Give the extent of all Plasmodium falciparum-infected red blood cells.
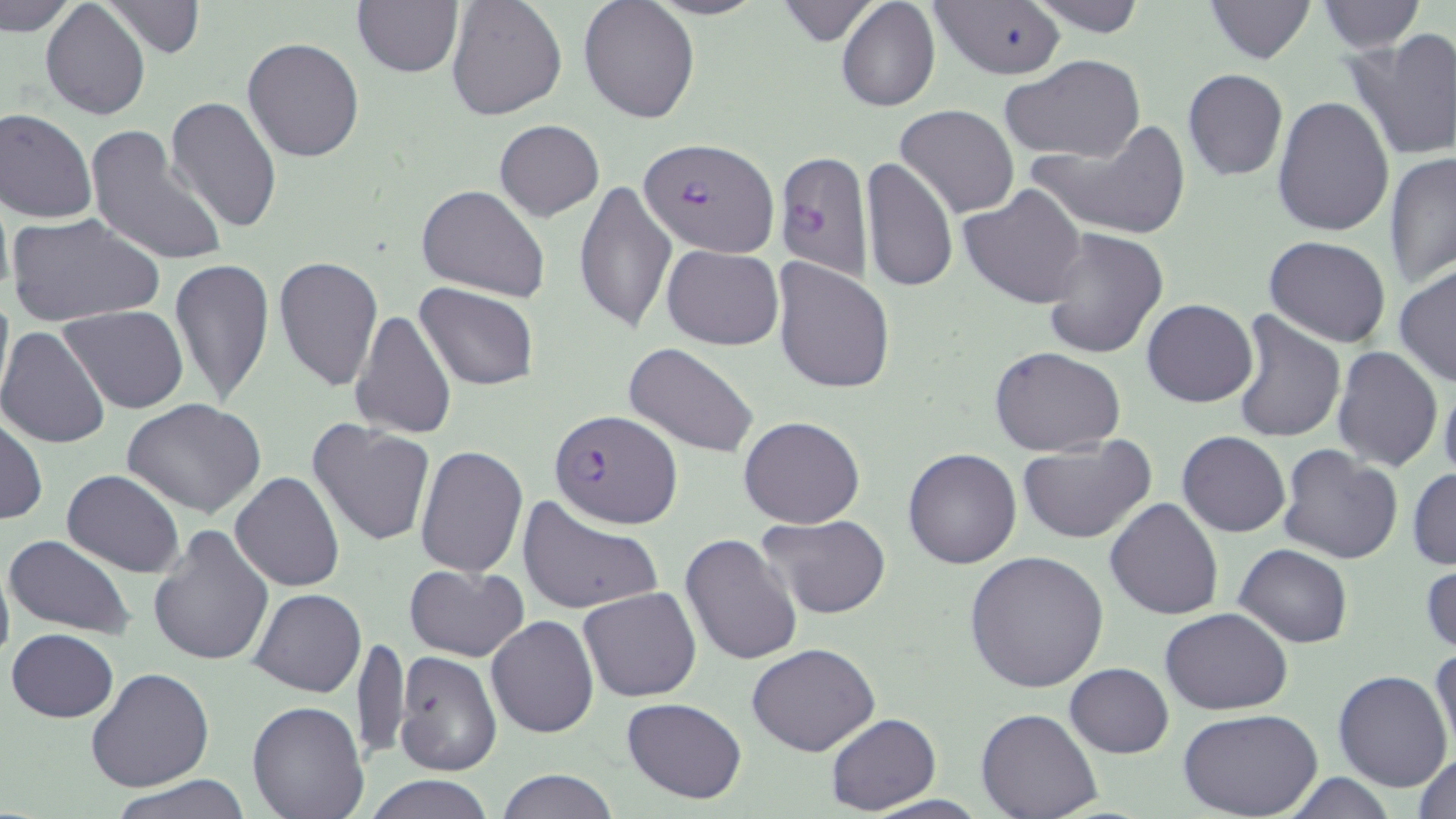
Approximate bounding boxes as named x1/y1/x2/y2 corners in pixels.
Plasmodium falciparum-infected red blood cells: (x1=642, y1=136, x2=778, y2=256), (x1=775, y1=151, x2=873, y2=281), (x1=549, y1=409, x2=682, y2=528).

Uninfected red blood cell locations: (x1=1, y1=0, x2=83, y2=36), (x1=101, y1=0, x2=205, y2=59), (x1=445, y1=0, x2=566, y2=122), (x1=578, y1=0, x2=700, y2=125), (x1=774, y1=0, x2=878, y2=41), (x1=835, y1=0, x2=941, y2=113), (x1=931, y1=0, x2=1066, y2=80), (x1=1027, y1=0, x2=1151, y2=36), (x1=1206, y1=0, x2=1313, y2=63), (x1=352, y1=1, x2=463, y2=79), (x1=1316, y1=1, x2=1424, y2=52), (x1=41, y1=2, x2=150, y2=119), (x1=1346, y1=30, x2=1456, y2=162), (x1=242, y1=37, x2=365, y2=162), (x1=1000, y1=57, x2=1148, y2=164), (x1=1182, y1=69, x2=1288, y2=180), (x1=1272, y1=94, x2=1396, y2=237), (x1=166, y1=96, x2=283, y2=235), (x1=895, y1=104, x2=1019, y2=219), (x1=0, y1=107, x2=98, y2=224), (x1=495, y1=119, x2=605, y2=221), (x1=1027, y1=123, x2=1193, y2=240), (x1=84, y1=125, x2=230, y2=267), (x1=1385, y1=151, x2=1456, y2=287), (x1=861, y1=156, x2=958, y2=296), (x1=574, y1=179, x2=677, y2=336), (x1=416, y1=184, x2=549, y2=301), (x1=960, y1=184, x2=1089, y2=307), (x1=6, y1=213, x2=164, y2=329), (x1=1040, y1=228, x2=1168, y2=360), (x1=1265, y1=237, x2=1392, y2=347), (x1=662, y1=245, x2=783, y2=348), (x1=274, y1=254, x2=383, y2=395), (x1=168, y1=257, x2=275, y2=406), (x1=772, y1=258, x2=895, y2=395), (x1=1395, y1=266, x2=1455, y2=388), (x1=416, y1=282, x2=540, y2=390), (x1=0, y1=285, x2=14, y2=412), (x1=1142, y1=298, x2=1258, y2=408), (x1=61, y1=306, x2=187, y2=414), (x1=351, y1=309, x2=457, y2=441), (x1=1231, y1=311, x2=1346, y2=445), (x1=0, y1=325, x2=114, y2=450), (x1=625, y1=342, x2=760, y2=459), (x1=1332, y1=345, x2=1443, y2=471), (x1=991, y1=347, x2=1126, y2=457), (x1=1439, y1=376, x2=1456, y2=484), (x1=123, y1=400, x2=266, y2=516), (x1=0, y1=416, x2=46, y2=525), (x1=739, y1=416, x2=866, y2=529), (x1=307, y1=420, x2=437, y2=548), (x1=1178, y1=431, x2=1290, y2=537), (x1=1016, y1=437, x2=1155, y2=544), (x1=414, y1=443, x2=526, y2=580), (x1=1278, y1=444, x2=1404, y2=566), (x1=903, y1=448, x2=1021, y2=569), (x1=1409, y1=467, x2=1456, y2=571), (x1=61, y1=468, x2=184, y2=577), (x1=230, y1=472, x2=343, y2=592), (x1=516, y1=494, x2=663, y2=616), (x1=1105, y1=497, x2=1223, y2=619), (x1=756, y1=514, x2=891, y2=619), (x1=147, y1=525, x2=275, y2=668), (x1=680, y1=531, x2=803, y2=667), (x1=4, y1=534, x2=135, y2=639), (x1=1235, y1=543, x2=1351, y2=648), (x1=966, y1=549, x2=1109, y2=693), (x1=0, y1=553, x2=14, y2=673), (x1=1421, y1=553, x2=1455, y2=661), (x1=404, y1=562, x2=528, y2=661), (x1=579, y1=586, x2=702, y2=703), (x1=249, y1=588, x2=365, y2=697), (x1=1161, y1=607, x2=1292, y2=713), (x1=486, y1=614, x2=597, y2=739), (x1=7, y1=628, x2=119, y2=723), (x1=352, y1=634, x2=408, y2=767), (x1=747, y1=641, x2=879, y2=756), (x1=1429, y1=645, x2=1456, y2=759), (x1=393, y1=651, x2=502, y2=776), (x1=1065, y1=662, x2=1173, y2=757), (x1=86, y1=668, x2=214, y2=792), (x1=1333, y1=669, x2=1452, y2=791), (x1=622, y1=697, x2=748, y2=803), (x1=247, y1=701, x2=370, y2=819), (x1=977, y1=709, x2=1103, y2=819), (x1=1181, y1=711, x2=1321, y2=819), (x1=825, y1=713, x2=940, y2=814), (x1=1412, y1=750, x2=1456, y2=819), (x1=494, y1=769, x2=619, y2=819), (x1=1276, y1=773, x2=1401, y2=817), (x1=109, y1=774, x2=253, y2=818), (x1=363, y1=774, x2=495, y2=818). Slide-level diagnosis: Plasmodium falciparum. May-Grünwald-Giemsa stain. Thin blood film. Image is 1456×819 pixels. One field of a larger specimen. Optical microscopy. Captured at 1000x magnification.